Classify this cell by malaria status.
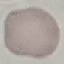

Uninfected.

Cell patch, automatically extracted from a larger field of view and resized to 64 × 64 pixels. Giemsa stain. Thin blood film. Photographed with a smartphone camera at the microscope eyepiece.